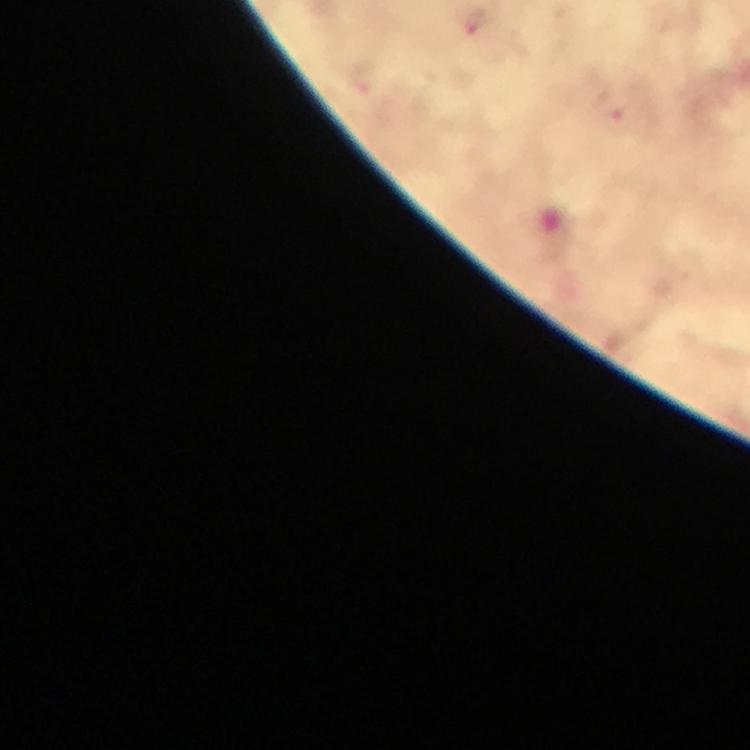
{
  "immersion_oil": "applied",
  "cropped_from": "a single field of view",
  "magnification": "100x",
  "capture": "smartphone photograph through a microscope",
  "stain": "Giemsa",
  "image_size": "750×750 pixels",
  "preparation": "thick smear",
  "malaria_parasite_locations": "approximate centers as (x, y) in pixels: (475, 24), (617, 116)",
  "context": "from a diagnostic examination for malaria"
}